Classify this cell by malaria status.
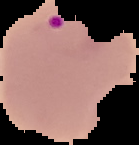

Parasitized.

Summary:
  - Preparation: thin blood smear
  - Image type: cell region segmented out of the field of view; surrounding area masked to black
  - Image size: 139×145 pixels